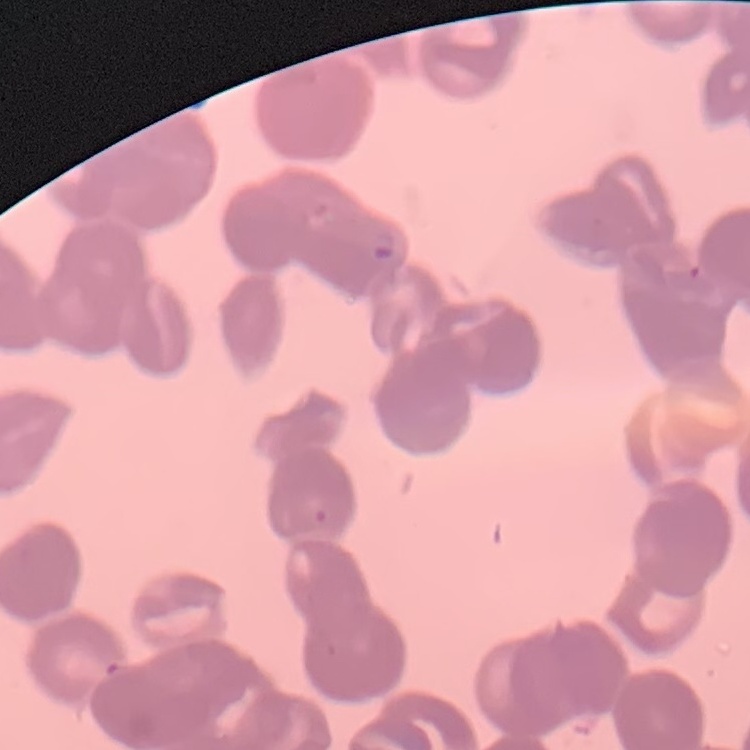
erythrocyte morphology = rouleaux formation
image type = one tile cut from a larger photomicrograph
stain = Field's or Giemsa
preparation = thin blood smear